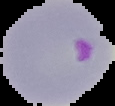
Summary:
  - Image size: 115×106 pixels
  - Image type: segmented cell region with the area outside set to black
  - Preparation: thin blood film
  - Malaria status: parasitized